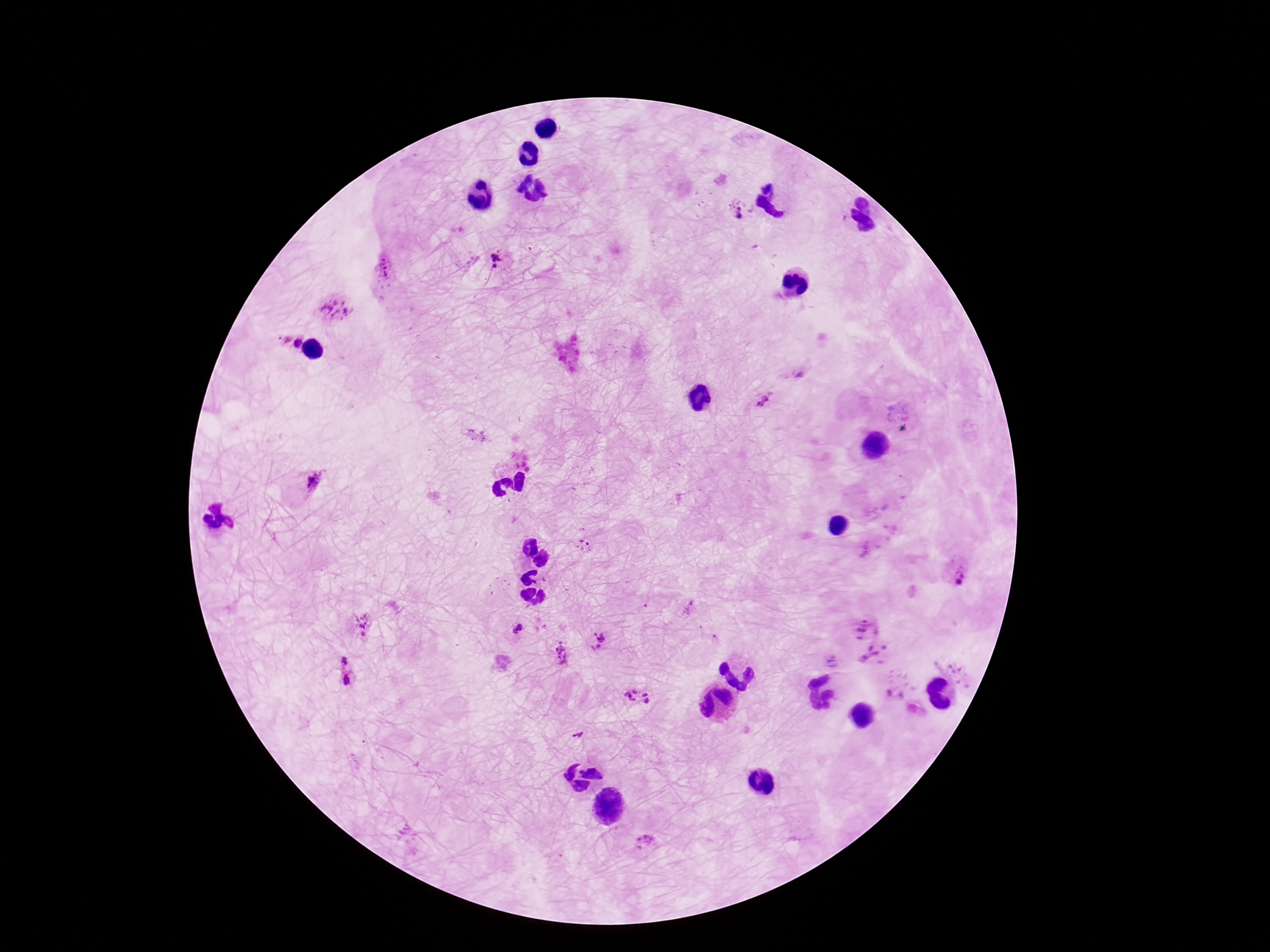
Approximate centers as [x, y] in pixels.
Summary:
  - Plasmodium parasite locations: [736, 212], [501, 262], [385, 269], [332, 308], [292, 342], [795, 374], [764, 400], [905, 423], [313, 482], [956, 571], [362, 624], [865, 627], [519, 631], [601, 642], [562, 653], [874, 658], [346, 672], [639, 698], [644, 842]
  - Capture: smartphone camera through the microscope eyepiece
  - Preparation: thick blood smear
  - Magnification: 100x
  - Patient malaria status: infected
  - Stain: Giemsa
  - Field of view: one from this slide
  - Image size: 1270×952 pixels